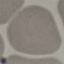

Summary:
  - Malaria status: uninfected
  - Stain: Giemsa
  - Image type: automatically extracted cell patch, resized to 64 × 64 pixels
  - Preparation: thin smear
  - Capture: smartphone through the microscope eyepiece